Give the position of every Plasmodium parasite.
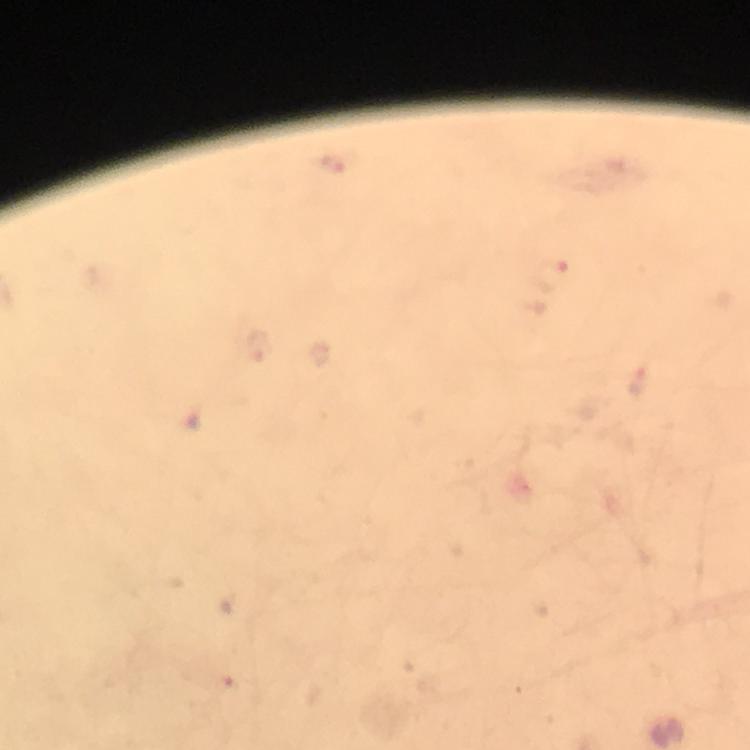
Approximate object centers, in pixels from the top-left corner.
Plasmodium parasites: (x=553, y=275).

Summary:
  - Immersion oil: applied
  - Magnification: 100x
  - Image size: 750×750 pixels
  - Preparation: thick smear
  - Context: from a diagnostic examination for malaria
  - Stain: Giemsa
  - Cropped from: a single field of view
  - Capture: smartphone photograph through a microscope